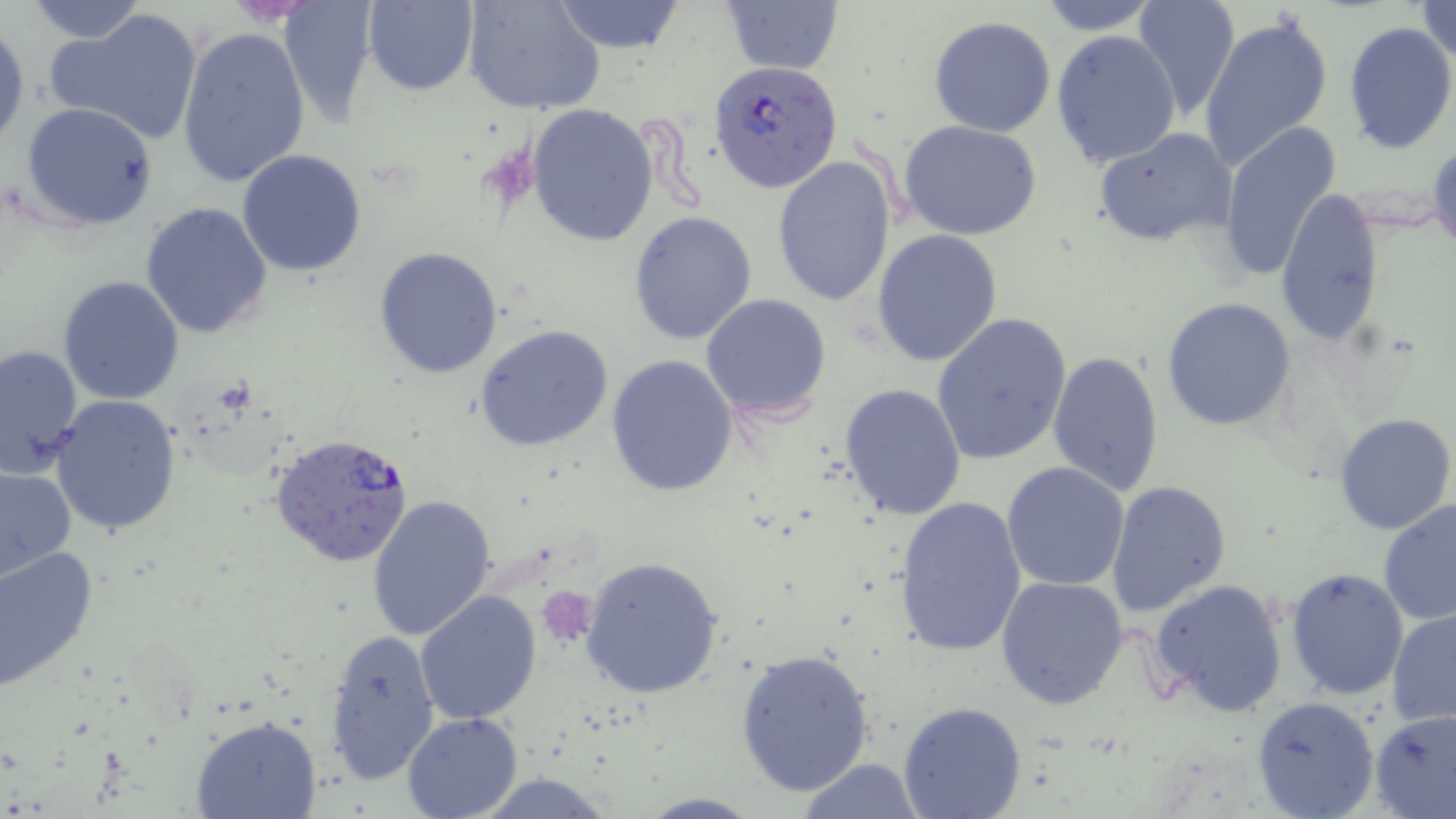 Approximate bounding boxes as [x1, y1, x2, y2] in pixels. Platelet locations: [538, 586, 598, 646]. Uninfected red blood cell locations: [278, 0, 380, 123], [360, 0, 478, 93], [463, 0, 605, 116], [552, 0, 686, 53], [719, 0, 844, 73], [1037, 0, 1162, 34], [1132, 0, 1240, 119], [25, 1, 148, 43], [1417, 2, 1455, 61], [46, 8, 204, 147], [1199, 14, 1334, 173], [929, 16, 1056, 137], [1341, 21, 1456, 155], [0, 25, 27, 151], [177, 26, 309, 188], [1050, 30, 1182, 168], [22, 102, 158, 231], [526, 104, 659, 248], [1216, 120, 1344, 281], [899, 121, 1044, 241], [1094, 126, 1237, 248], [237, 150, 368, 278], [771, 156, 898, 307], [1275, 189, 1386, 348], [139, 202, 272, 338], [628, 211, 759, 345], [871, 228, 1004, 367], [374, 245, 505, 379], [58, 275, 186, 406], [701, 293, 833, 421], [1161, 298, 1297, 431], [932, 313, 1071, 465], [475, 325, 615, 453], [0, 341, 83, 478], [1048, 351, 1166, 496], [606, 355, 738, 496], [838, 382, 968, 521], [50, 395, 184, 536], [1334, 411, 1456, 535], [1002, 461, 1131, 592], [0, 465, 76, 581], [1105, 480, 1232, 618], [366, 493, 495, 642], [895, 495, 1027, 658], [1378, 499, 1456, 629], [0, 545, 99, 691], [578, 557, 725, 701], [1283, 567, 1409, 702], [996, 575, 1128, 709], [1151, 578, 1289, 717], [415, 590, 543, 725], [1387, 609, 1456, 731], [323, 627, 442, 785], [735, 647, 876, 798], [1251, 696, 1380, 819], [898, 701, 1027, 819], [1370, 708, 1456, 817], [403, 710, 523, 818], [190, 716, 323, 819], [793, 759, 929, 817]. Plasmodium falciparum-infected red blood cell locations: [709, 60, 843, 193], [267, 430, 416, 567]. Slide-level diagnosis: Plasmodium falciparum. Light microscopy. 1000x magnification. Image is 1456×819 pixels. Single field of view. Thin blood film. May-Grünwald-Giemsa stain.